Locate and identify every blood parasite.
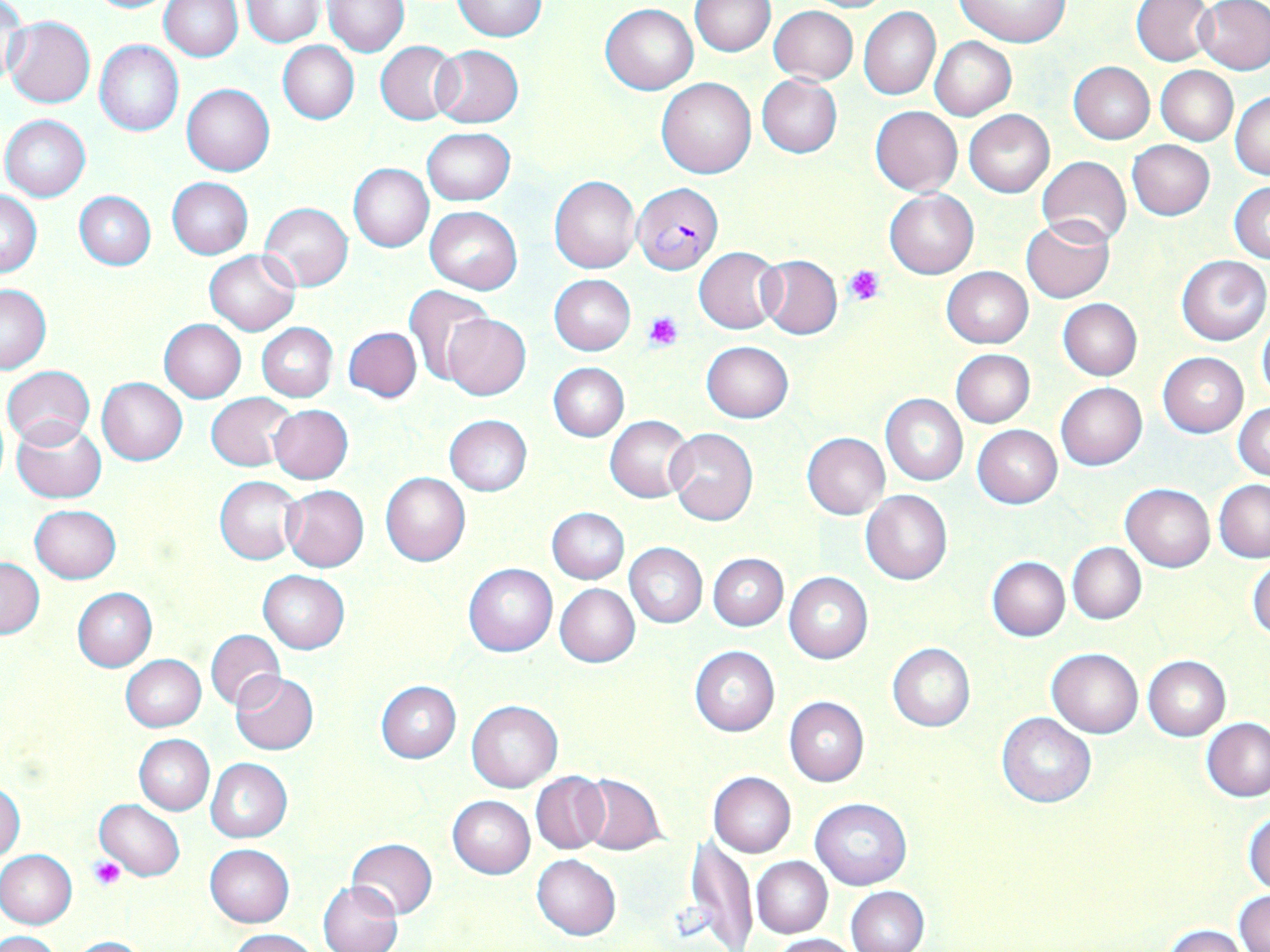
Approximate bounding boxes as (x1,y1)-(x2,y2) corner pairs in pixels.
Plasmodium falciparum-infected red blood cells: (631,182)-(723,276).
No Plasmodium ovale, Plasmodium malariae, Plasmodium vivax, Babesia divergens, or Trypanosoma brucei observed.

Uninfected red blood cell locations: (2,0)-(28,88), (82,0)-(182,14), (159,0)-(243,61), (242,0)-(324,45), (324,0)-(409,55), (956,0)-(1068,47), (1132,0)-(1215,66), (453,1)-(547,40), (689,1)-(776,56), (798,1)-(897,13), (1196,1)-(1270,74), (601,3)-(698,94), (769,6)-(858,85), (859,7)-(940,100), (4,16)-(96,108), (930,36)-(1017,120), (94,41)-(183,136), (278,41)-(359,124), (376,42)-(460,123), (431,45)-(524,128), (1068,61)-(1155,144), (1155,66)-(1238,145), (757,75)-(842,158), (657,77)-(757,179), (182,83)-(274,176), (1231,92)-(1269,180), (870,106)-(961,195), (964,109)-(1056,197), (1,115)-(91,200), (422,127)-(515,205), (1127,140)-(1214,220), (1037,156)-(1131,247), (349,163)-(434,252), (550,175)-(641,274), (167,178)-(253,258), (1228,182)-(1270,263), (1,190)-(41,277), (73,190)-(156,270), (885,190)-(979,279), (259,203)-(353,292), (424,206)-(522,294), (1022,218)-(1115,302), (695,247)-(782,334), (204,249)-(300,335), (757,255)-(842,339), (1177,255)-(1269,345), (942,267)-(1033,348), (549,275)-(636,354), (0,284)-(52,373), (405,286)-(494,382), (1057,298)-(1141,380), (441,311)-(532,402), (1256,318)-(1270,403), (158,320)-(246,403), (257,323)-(337,402), (344,326)-(421,403), (701,340)-(794,421), (950,348)-(1035,427), (1158,352)-(1247,437), (550,363)-(628,441), (2,366)-(94,449), (97,377)-(188,465), (1055,382)-(1147,470), (207,392)-(294,471), (880,394)-(968,485), (1233,403)-(1270,480), (267,404)-(353,484), (444,415)-(532,495), (605,415)-(693,502), (13,419)-(107,503), (973,425)-(1062,508), (665,427)-(758,524), (803,432)-(890,518), (380,472)-(470,566), (216,476)-(304,564), (1215,480)-(1270,561), (1121,484)-(1215,572), (282,485)-(369,572), (861,490)-(953,584), (29,504)-(121,582), (546,506)-(629,583), (624,542)-(707,628), (1067,543)-(1147,623), (709,553)-(787,631), (1,557)-(44,638), (986,557)-(1069,641), (1248,559)-(1270,641), (464,563)-(557,657), (258,570)-(350,653), (784,572)-(873,663), (555,583)-(640,667), (71,588)-(157,672), (205,629)-(284,709), (887,644)-(975,731), (690,647)-(778,736), (1046,648)-(1143,738), (121,655)-(205,730), (1143,656)-(1230,739), (230,671)-(318,755), (376,680)-(461,763), (785,697)-(869,786), (465,700)-(562,793), (996,711)-(1097,807), (1202,718)-(1269,801), (135,734)-(215,815), (206,757)-(292,842), (531,772)-(608,854), (707,772)-(795,857), (578,774)-(667,855), (1,783)-(25,862), (448,795)-(535,879), (811,798)-(911,890), (94,799)-(185,882), (1244,810)-(1270,895), (685,838)-(758,949), (346,839)-(437,919), (205,845)-(294,927), (0,849)-(77,928), (532,854)-(621,940), (752,856)-(832,938), (318,880)-(402,952), (846,886)-(929,952), (1233,892)-(1270,951), (1163,927)-(1249,952), (229,929)-(319,952), (1,930)-(64,952), (769,933)-(861,952), (65,935)-(152,951). Platelet locations: (844,265)-(884,305), (644,311)-(684,349), (89,858)-(127,890). Slide-level diagnosis: Plasmodium falciparum. One field of a larger specimen. Optical microscopy. Captured at 1000x magnification. May-Grünwald-Giemsa-stained preparation. Image is 1270×952 pixels. Thin blood smear.